Point out each malaria parasite and each leukocyte.
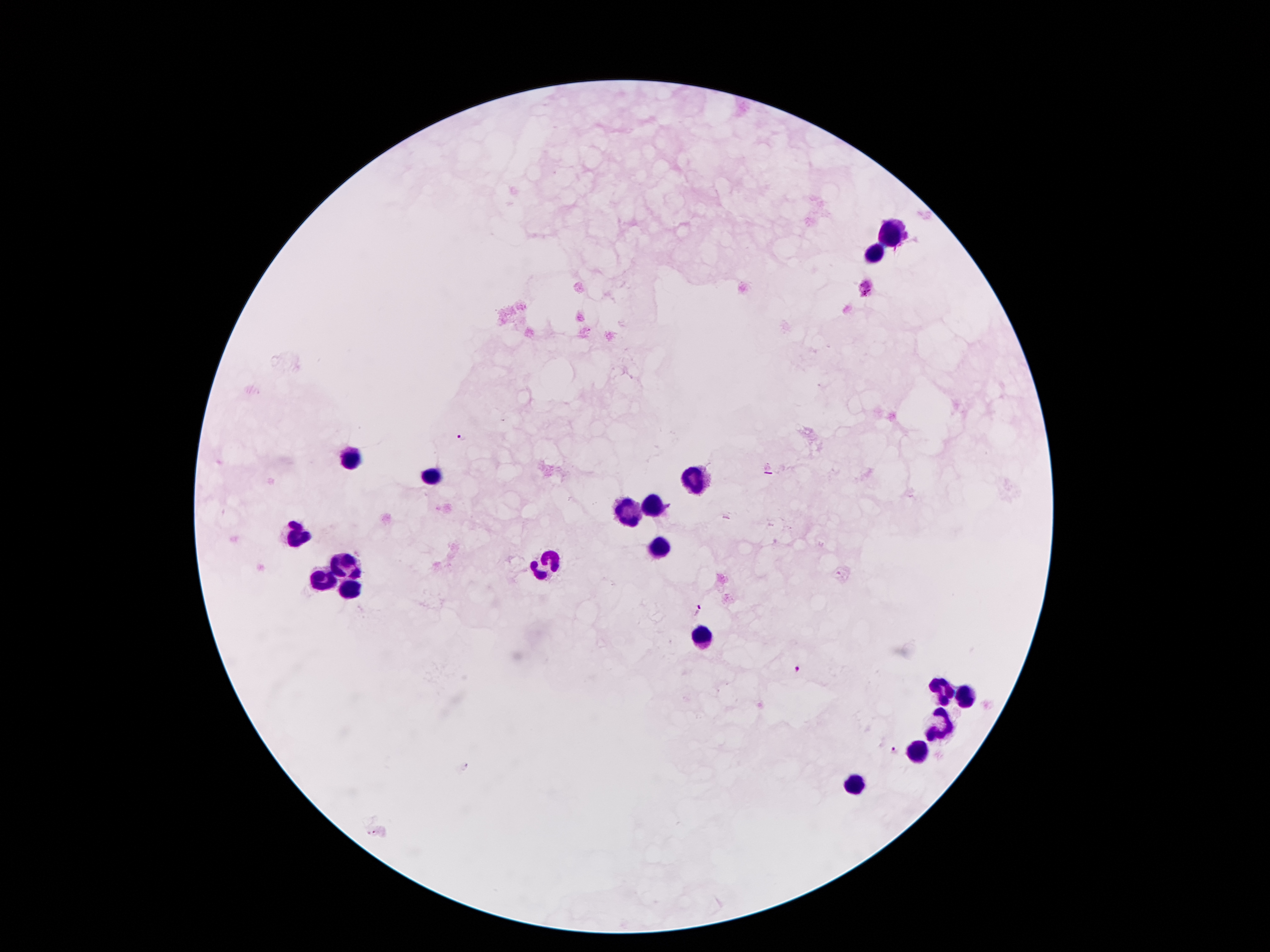

Approximate centers as [x, y] in pixels.
Malaria parasites: [460, 438], [697, 612], [797, 670], [893, 751], [373, 833].
Leukocytes: [889, 230], [875, 254], [346, 458], [430, 475], [695, 475], [651, 504], [630, 511], [294, 533], [659, 545], [546, 561], [342, 564], [322, 576], [349, 585], [702, 636], [942, 686], [963, 696], [942, 725], [918, 751], [858, 785].

Summary:
  - Magnification: 100x
  - Capture: smartphone camera through the microscope eyepiece
  - Image size: 1270×952 pixels
  - Patient malaria status: positive for Plasmodium falciparum
  - Preparation: thick blood film
  - Field of view: one from this slide
  - Stain: Giemsa